Point out each leukocyte.
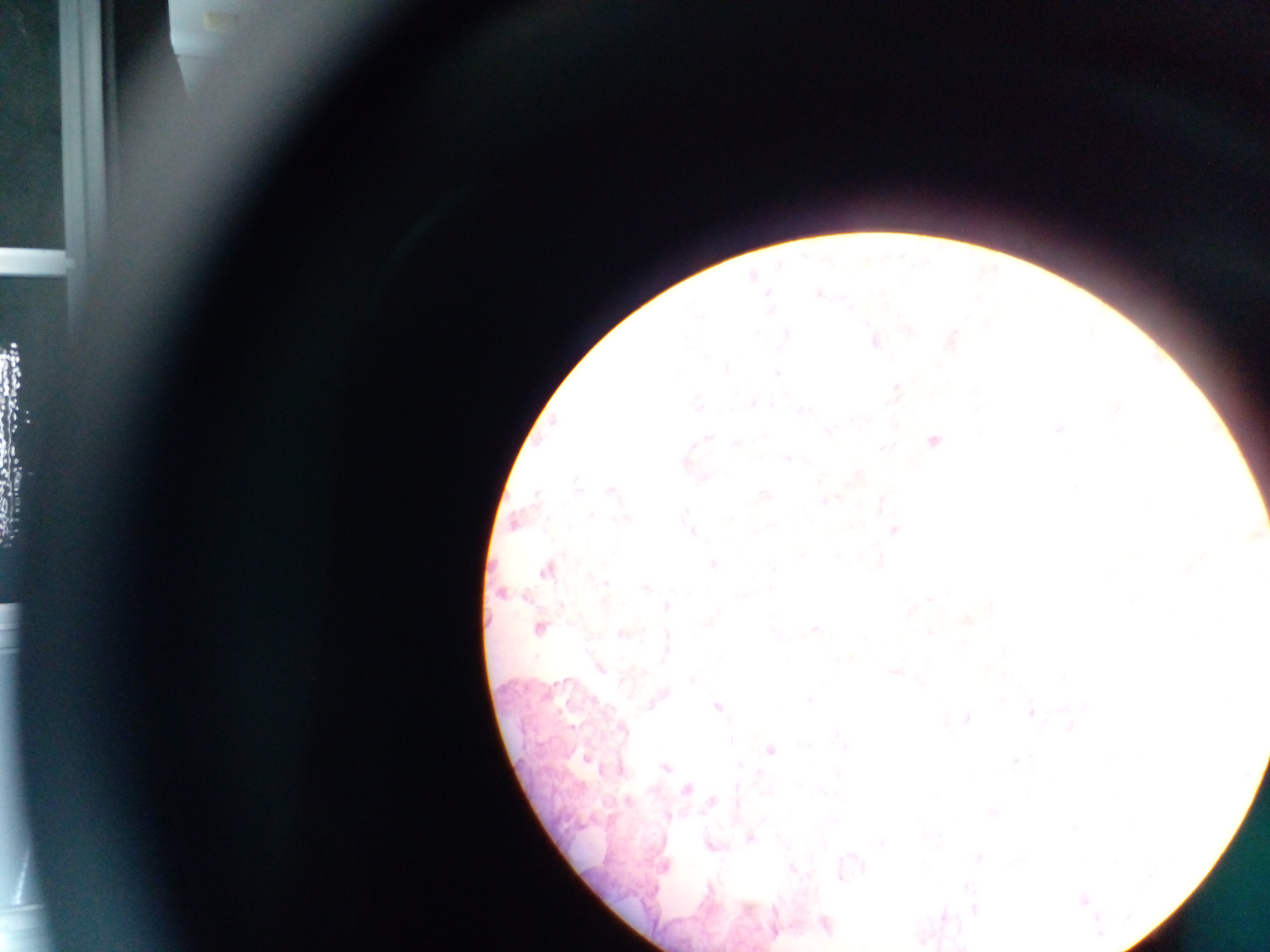

No leukocytes observed.

Approximate centers as (x, y) in pixels. Malaria parasite locations: (819, 294), (950, 338), (874, 341), (725, 368), (896, 390), (753, 403), (698, 406), (800, 409), (933, 439), (736, 442), (787, 456), (611, 490), (514, 523), (893, 530), (693, 532), (712, 564), (546, 569), (604, 583), (501, 592), (539, 627), (814, 629), (624, 632), (599, 666), (895, 670), (658, 697), (717, 707), (1031, 711), (966, 719), (770, 749), (585, 757), (665, 768), (685, 788), (712, 801), (750, 836), (711, 844), (977, 858), (1082, 900), (973, 909), (824, 925), (773, 930). Image is 1270×952 pixels. One field of view. Photographed through a microscope with a mobile-phone camera. Collected in Ghana. Thick blood smear.